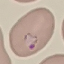

Result: malaria parasites identified. Cell patch, automatically extracted from a larger field of view and resized to 64 × 64 pixels. Thin blood smear. Acquired by smartphone through the microscope eyepiece. Giemsa-stained preparation.